Identify the parasite.
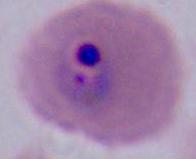

This is Plasmodium.

Summary:
  - Magnification: 400x or 1000x
  - Modality: micrograph